Give the extent of all uninfected red blood cells.
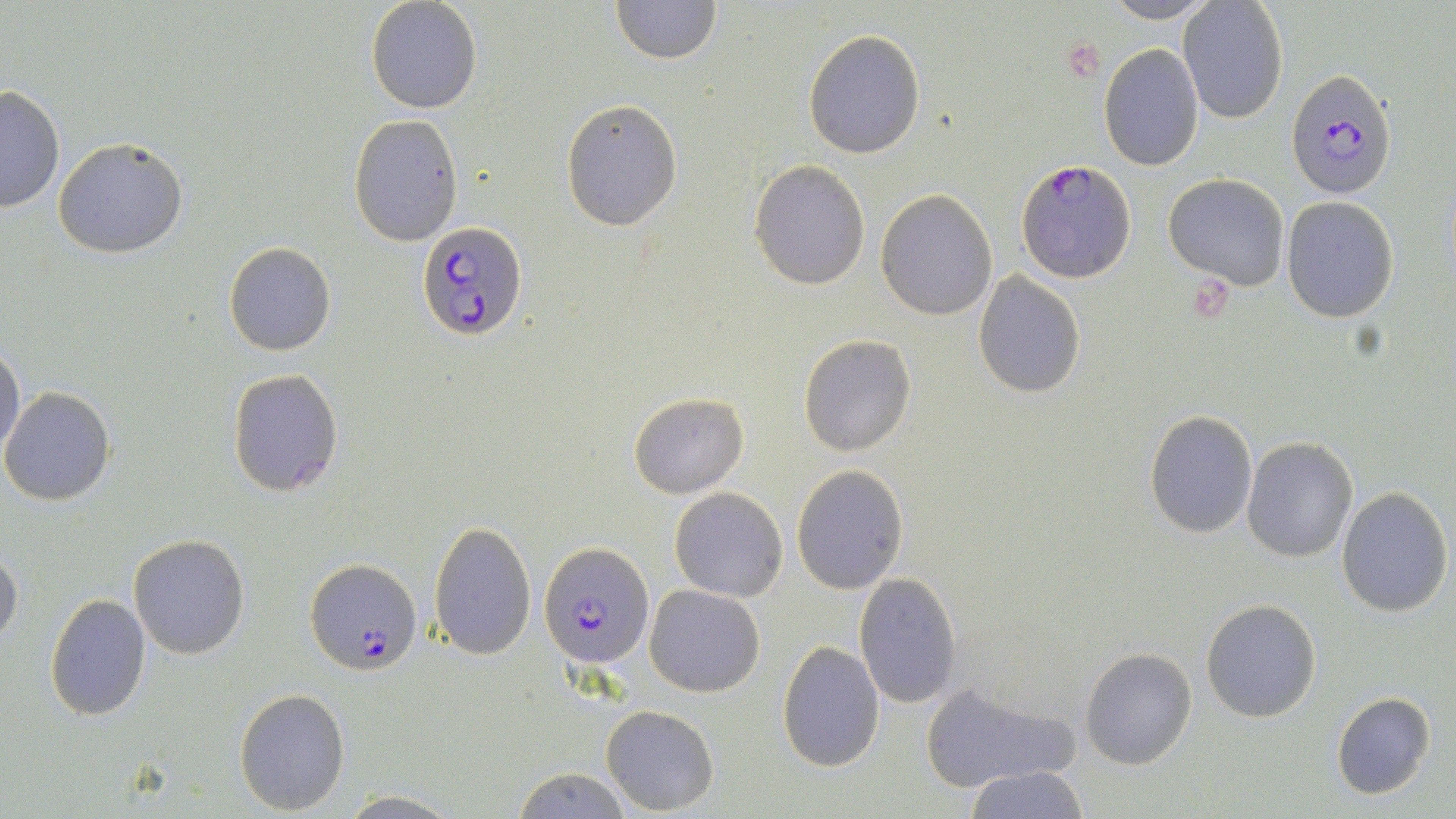
Approximate bounding boxes as named x1/y1/x2/y2 corners in pixels.
Uninfected red blood cells: (x1=366, y1=0, x2=482, y2=113), (x1=609, y1=0, x2=721, y2=65), (x1=1099, y1=0, x2=1221, y2=24), (x1=1178, y1=1, x2=1289, y2=125), (x1=803, y1=30, x2=925, y2=158), (x1=1098, y1=43, x2=1204, y2=170), (x1=0, y1=86, x2=65, y2=213), (x1=561, y1=97, x2=683, y2=231), (x1=349, y1=114, x2=463, y2=245), (x1=53, y1=136, x2=188, y2=259), (x1=749, y1=159, x2=872, y2=289), (x1=1163, y1=174, x2=1290, y2=291), (x1=875, y1=189, x2=998, y2=321), (x1=1282, y1=196, x2=1399, y2=322), (x1=224, y1=242, x2=335, y2=356), (x1=973, y1=270, x2=1086, y2=397), (x1=797, y1=335, x2=919, y2=457), (x1=0, y1=339, x2=25, y2=459), (x1=227, y1=369, x2=344, y2=497), (x1=1, y1=386, x2=116, y2=505), (x1=627, y1=391, x2=748, y2=497), (x1=1144, y1=407, x2=1257, y2=539), (x1=1243, y1=437, x2=1359, y2=561), (x1=791, y1=463, x2=909, y2=594), (x1=669, y1=487, x2=788, y2=602), (x1=1336, y1=487, x2=1453, y2=615), (x1=428, y1=520, x2=536, y2=657), (x1=128, y1=534, x2=250, y2=659), (x1=0, y1=549, x2=22, y2=648), (x1=853, y1=573, x2=962, y2=709), (x1=644, y1=584, x2=765, y2=697), (x1=44, y1=592, x2=152, y2=721), (x1=1200, y1=598, x2=1322, y2=722), (x1=777, y1=639, x2=884, y2=771), (x1=1079, y1=647, x2=1197, y2=769), (x1=917, y1=682, x2=1079, y2=792), (x1=233, y1=687, x2=352, y2=814), (x1=1330, y1=690, x2=1436, y2=800), (x1=602, y1=704, x2=719, y2=815), (x1=509, y1=766, x2=633, y2=818), (x1=963, y1=766, x2=1089, y2=819), (x1=338, y1=792, x2=461, y2=818).

slide-level diagnosis = Plasmodium falciparum
field of view = one of a larger specimen
preparation = thin blood smear
image size = 1456×819 pixels
stain = May-Grünwald-Giemsa
modality = light microscopy
Plasmodium falciparum-infected red blood cell locations = approximate bounding boxes as named x1/y1/x2/y2 corners in pixels: (x1=1285, y1=68, x2=1396, y2=197), (x1=1018, y1=160, x2=1136, y2=281), (x1=418, y1=218, x2=530, y2=342), (x1=540, y1=542, x2=653, y2=667), (x1=305, y1=558, x2=422, y2=675)
magnification = 1000x